Assess the morphology of the erythrocytes.
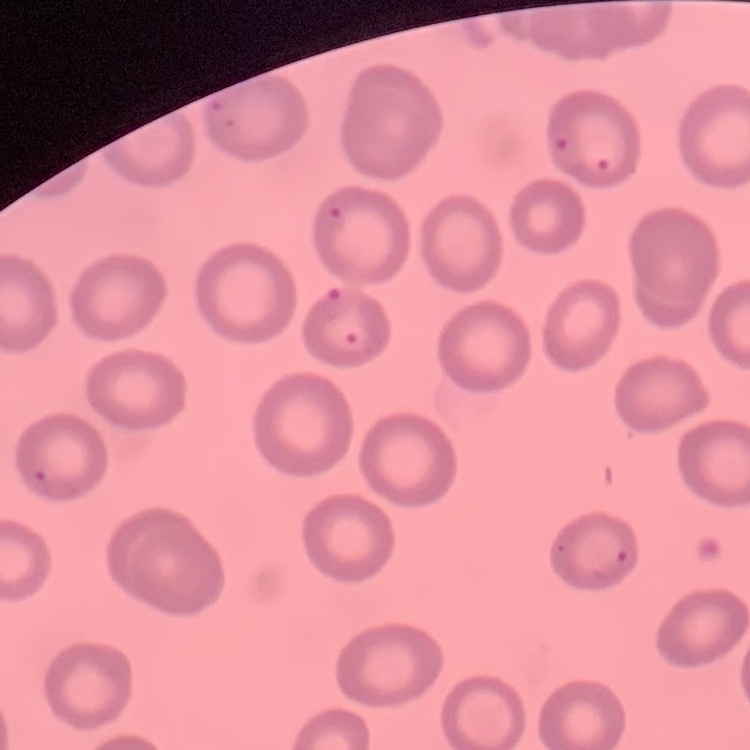

No rouleaux formation.

Summary:
  - Stain: Field's or Giemsa
  - Preparation: thin blood smear
  - Image type: one tile cut from a larger photomicrograph